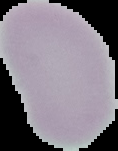

image_size: 118×151 pixels
malaria_status: uninfected
image_type: segmented cell region with the area outside set to black
preparation: thin blood film